Assess the morphology of the erythrocytes.
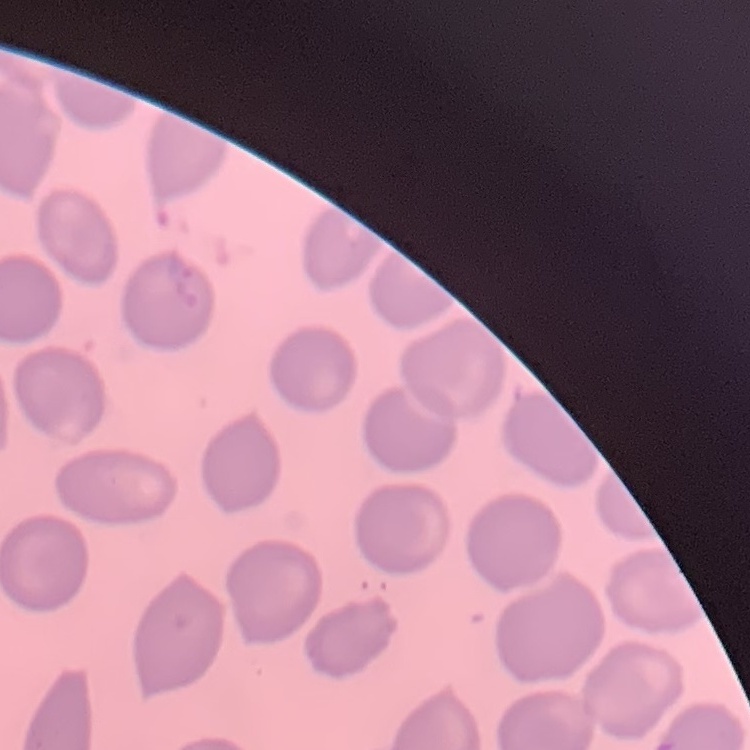
No rouleaux formation.

One tile cut from a larger photomicrograph. Stained with either Field's or Giemsa. Thin blood film.